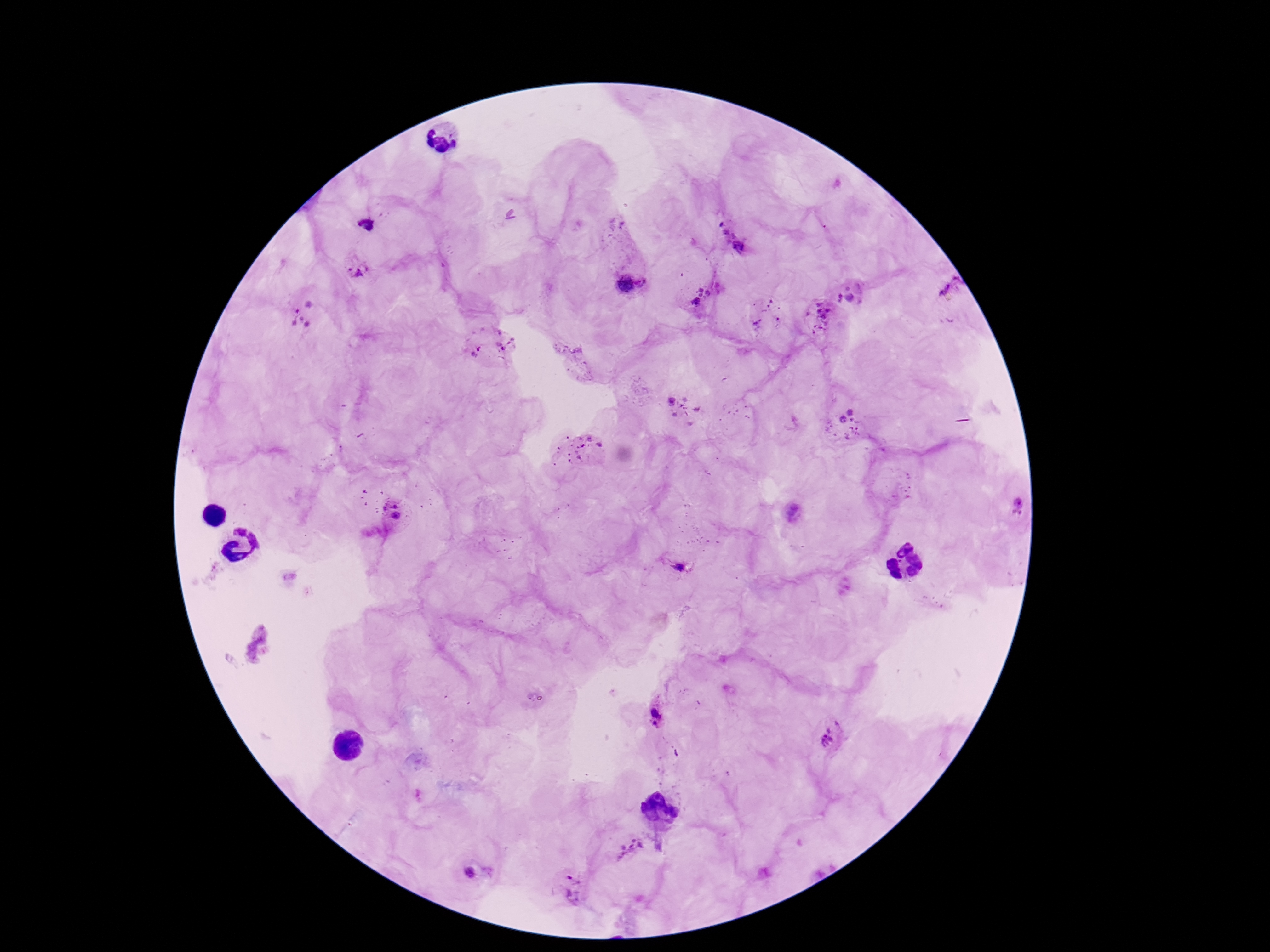
Approximate centers as [x, y] in pixels.
Summary:
  - Plasmodium parasite locations: [367, 225], [734, 240], [357, 271], [631, 284], [952, 286], [849, 294], [702, 297], [301, 313], [821, 314], [490, 342], [683, 408], [850, 424], [577, 447], [1020, 506], [395, 511], [676, 564], [657, 713], [833, 739], [632, 847], [477, 870], [573, 887]
  - Preparation: thick blood film
  - Field of view: one from this slide
  - Image size: 1270×952 pixels
  - Magnification: 100x
  - Patient malaria status: positive
  - Stain: Giemsa
  - Capture: smartphone camera through the microscope eyepiece